Locate the red blood cells and classify each one as Plasmodium falciparum-infected, uninfected, or of indeterminate infection status.
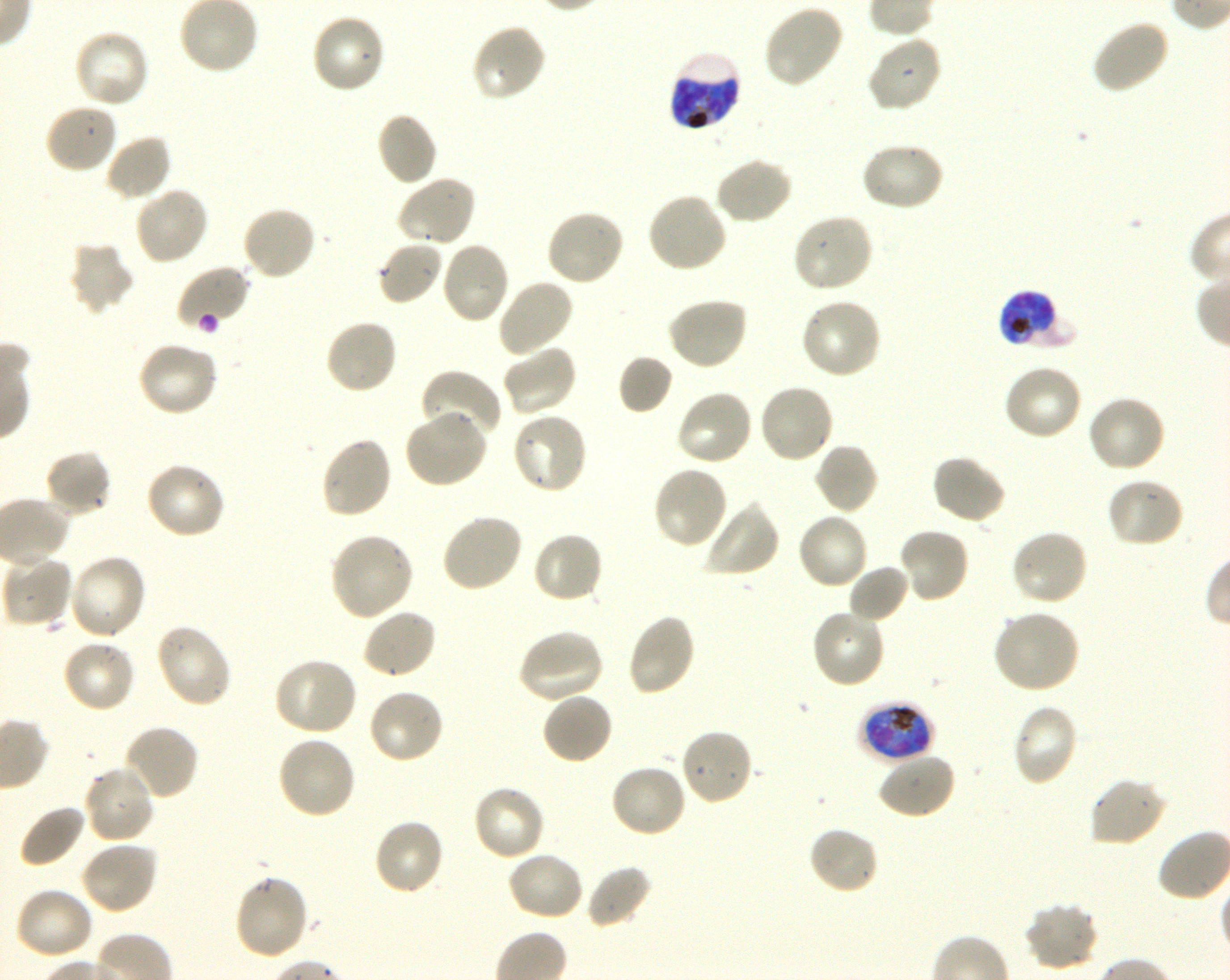
Approximate bounding boxes as (x1, y1, x2, y2) in pixels. Not every red blood cell is marked. A life-cycle stage — or a range of stages, where the recorded stages span more than one — follows each staged infected red blood cell.
Infected red blood cells: (668, 49, 743, 133) late trophozoite to late schizont; (998, 290, 1076, 350) early trophozoite to late schizont; (859, 700, 936, 764) late trophozoite to early schizont.
Uninfected red blood cells: (762, 3, 846, 89), (309, 13, 388, 95), (1091, 17, 1171, 95), (470, 23, 547, 104), (72, 28, 150, 110), (866, 34, 943, 114), (43, 103, 119, 176), (376, 111, 438, 186), (104, 134, 173, 202), (859, 141, 946, 213), (714, 156, 793, 226), (396, 173, 477, 248), (133, 186, 210, 266), (646, 190, 729, 275), (241, 205, 318, 281), (544, 208, 626, 287), (791, 212, 874, 294), (376, 240, 444, 307), (67, 241, 136, 316), (439, 241, 511, 324), (175, 264, 251, 330), (496, 277, 575, 358), (665, 296, 750, 372), (799, 297, 883, 380), (324, 318, 398, 396), (136, 340, 220, 417), (501, 344, 578, 417), (618, 354, 673, 414), (1003, 364, 1084, 442), (420, 369, 502, 443), (758, 384, 835, 465), (674, 388, 754, 466), (1087, 395, 1167, 474), (403, 409, 489, 490), (510, 412, 589, 495), (320, 435, 393, 519), (813, 442, 880, 515), (43, 448, 112, 519), (931, 454, 1007, 526), (144, 461, 226, 541), (652, 465, 729, 550), (1106, 477, 1184, 549), (703, 501, 780, 578), (440, 512, 523, 593), (796, 512, 869, 591), (898, 525, 971, 604), (1010, 528, 1090, 608), (531, 530, 604, 605), (329, 531, 415, 622), (67, 553, 148, 642), (10, 555, 72, 628), (847, 564, 910, 624), (361, 607, 437, 679), (810, 608, 886, 689), (992, 609, 1082, 694), (626, 612, 697, 697), (154, 623, 233, 709), (517, 629, 605, 705), (61, 638, 137, 714), (273, 658, 358, 737), (367, 688, 446, 766), (540, 691, 614, 766), (1011, 703, 1079, 787), (122, 723, 199, 801), (678, 728, 754, 807), (276, 736, 358, 820), (876, 752, 957, 821), (609, 763, 689, 839), (82, 765, 156, 845), (1089, 777, 1167, 847), (471, 783, 547, 862), (18, 804, 86, 869), (371, 818, 445, 897), (807, 824, 881, 895), (79, 839, 160, 916), (505, 850, 585, 922), (585, 864, 653, 929), (232, 874, 310, 961), (13, 886, 94, 961), (1024, 901, 1100, 972).
No red blood cells of indeterminate infection status observed.

Blood group of the donor: O+. 100x objective under oil immersion, numerical aperture 1.30. One field from this slide. Thin blood smear. Image is 1230×980 pixels. Plasmodium falciparum strain 3D7 in shaking in-vitro culture. Giemsa stain.